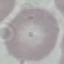

Summary:
  - Malaria status: uninfected
  - Preparation: thin blood smear
  - Stain: Giemsa
  - Capture: smartphone camera at the microscope eyepiece
  - Image type: cell patch, automatically extracted from a larger field of view and resized to 64 × 64 pixels